Locate malaria parasites and leukocytes.
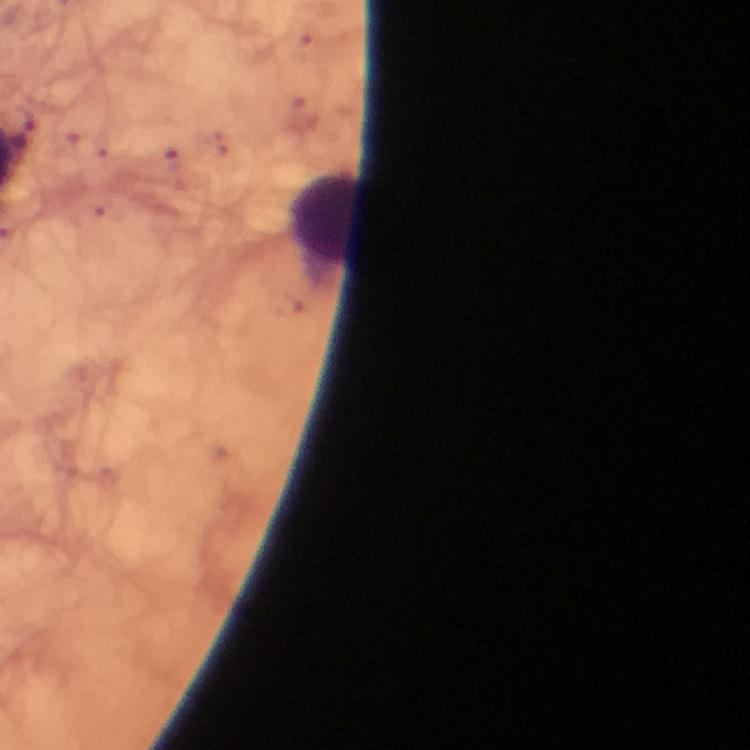

No malaria parasites detected.
Approximate object centers, in pixels from the top-left corner.
Leukocytes: (x=326, y=218).

Summary:
  - Image size: 750×750 pixels
  - Cropped from: one field of view
  - Preparation: thick blood film
  - Immersion oil: applied
  - Stain: Giemsa
  - Capture: smartphone mounted on the microscope
  - Context: from a malaria diagnostic workup
  - Magnification: 100x